Assess the morphology of the red blood cells.
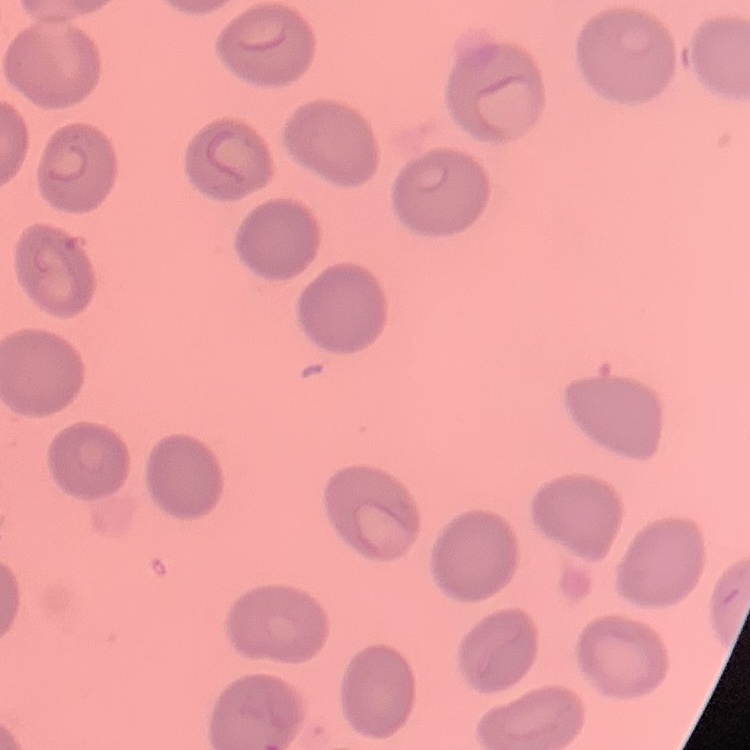
No rouleaux formation.

preparation = thin blood smear
image type = square crop of a larger photomicrograph
stain = Field's or Giemsa